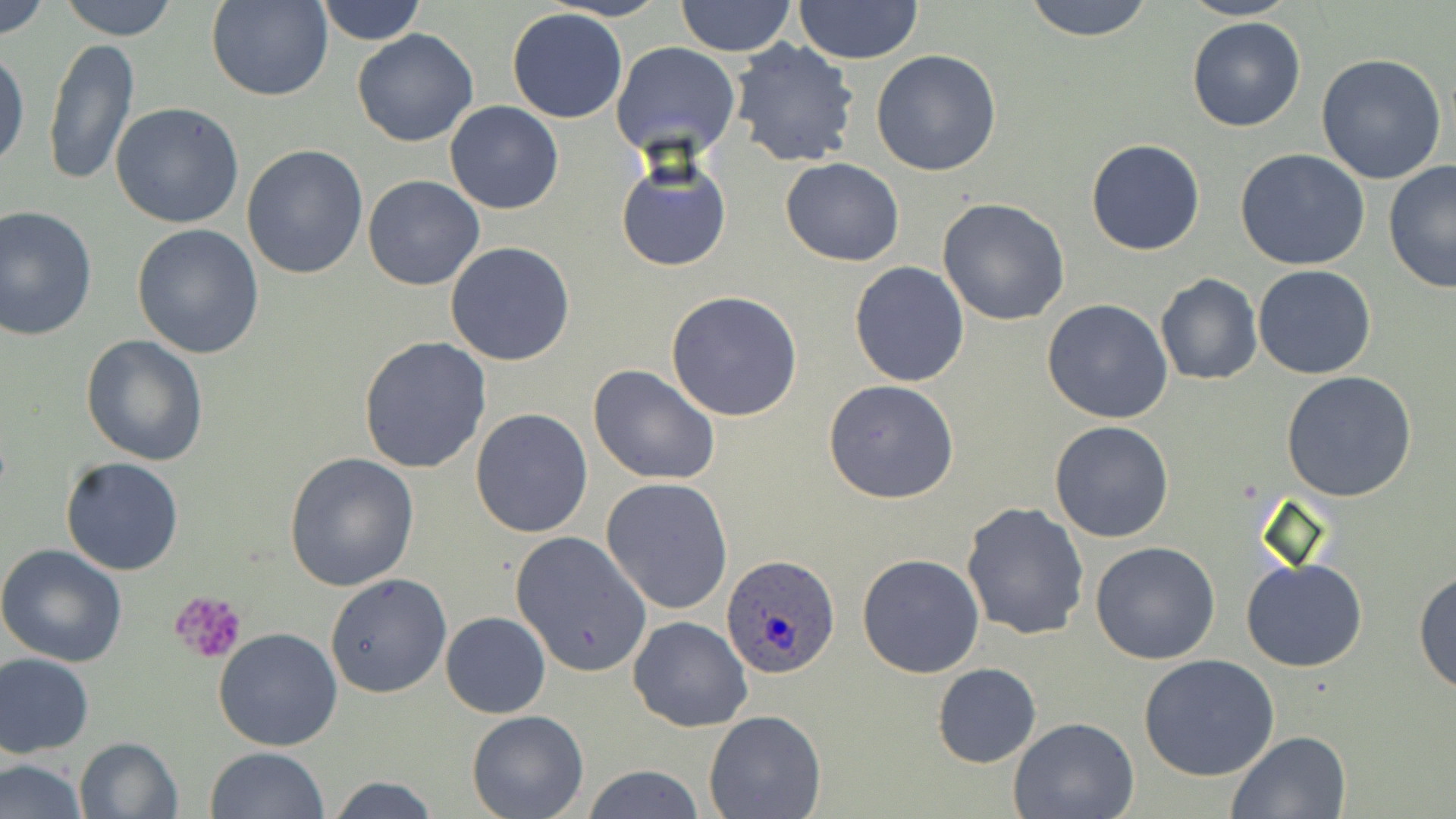

Summary:
  - Coordinate format: approximate bounding boxes as (x1,y1)-(x2,y2) corner pairs in pixels
  - Uninfected red blood cell locations: (0,0)-(52,42), (58,0)-(179,42), (206,0)-(332,102), (314,0)-(427,46), (544,0)-(672,21), (674,0)-(797,57), (1021,0)-(1156,40), (1181,0)-(1299,22), (793,1)-(925,64), (507,8)-(628,124), (1186,16)-(1306,132), (352,28)-(479,147), (44,36)-(139,189), (727,39)-(861,170), (611,42)-(741,161), (0,45)-(29,174), (871,49)-(1001,177), (1314,53)-(1447,184), (111,102)-(245,230), (445,102)-(564,215), (1085,137)-(1207,256), (242,145)-(369,281), (1235,149)-(1371,271), (616,157)-(733,272), (780,158)-(904,267), (1382,162)-(1456,294), (363,175)-(485,290), (937,198)-(1070,326), (0,206)-(97,340), (132,223)-(264,359), (445,241)-(577,366), (848,260)-(970,388), (1252,265)-(1376,380), (1155,273)-(1262,386), (666,291)-(803,423), (1043,298)-(1173,424), (80,334)-(209,465), (358,336)-(491,473), (588,362)-(721,486), (1281,372)-(1421,504), (822,379)-(961,503), (470,408)-(594,539), (1049,421)-(1174,542), (283,453)-(420,592), (60,455)-(185,575), (600,477)-(734,614), (961,502)-(1089,639), (507,529)-(651,677), (1090,541)-(1222,665), (0,544)-(128,666), (857,554)-(983,676), (1241,558)-(1368,672), (1413,568)-(1456,695), (325,573)-(453,699), (440,611)-(550,718), (628,615)-(753,732), (213,626)-(344,751), (0,653)-(95,757), (1138,654)-(1281,782), (932,663)-(1041,767), (466,710)-(588,819), (704,711)-(825,819), (1010,717)-(1139,818), (1227,730)-(1351,818), (73,736)-(182,818), (205,746)-(330,819), (0,757)-(88,818), (578,764)-(706,819), (322,776)-(443,818)
  - Plasmodium ovale-infected red blood cell locations: (723,554)-(840,678)
  - Platelet locations: (168,590)-(248,664)
  - Slide-level diagnosis: Plasmodium ovale
  - Modality: light microscopy
  - Magnification: 1000x
  - Stain: May-Grünwald-Giemsa
  - Preparation: thin blood smear
  - Image size: 1456×819 pixels
  - Field of view: one of a larger specimen